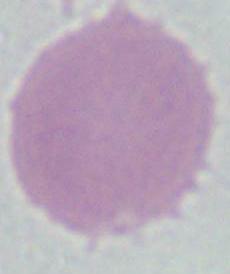

Captured at 1000x magnification. A red blood cell is shown. Micrograph.